Assess for Plasmodium parasites.
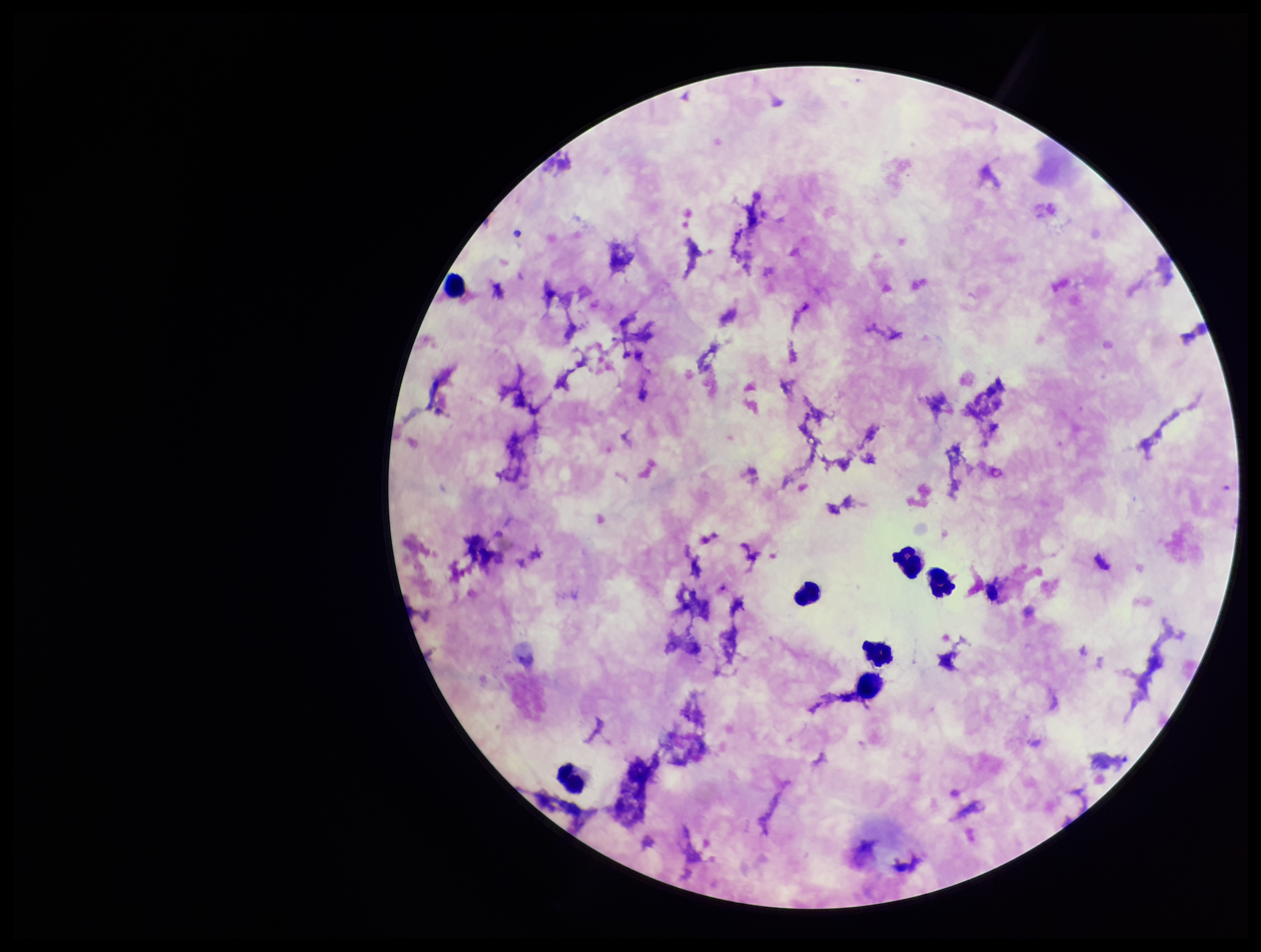
None detected.

Summary:
  - Species reported for this patient: Plasmodium falciparum
  - Stain: Giemsa
  - Leukocyte count: 7
  - Field of view: one from this slide
  - Parasite count: 0
  - Preparation: thick
  - Patient malaria status: infected
  - Image size: 1261×952 pixels
  - Capture: smartphone photograph through the microscope eyepiece